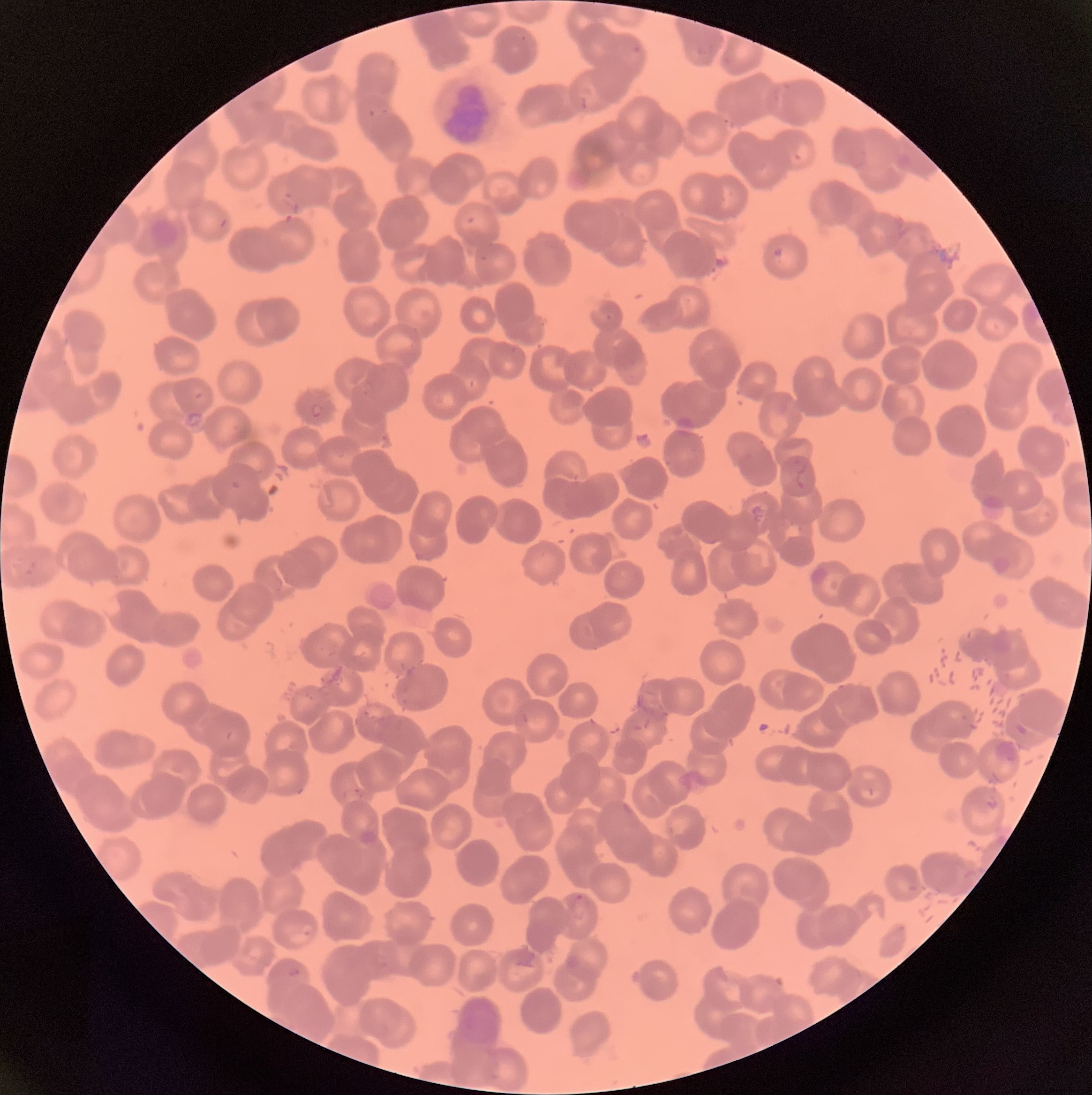

coordinate format = approximate bounding boxes as (x1,y1)-(x2,y2) corner pairs in pixels
Plasmodium parasite locations = (631,44)-(644,57), (368,109)-(376,118), (310,402)-(324,418), (569,893)-(591,920), (288,968)-(300,978)
red blood cell morphology = rouleaux formation
image size = 1092×1095 pixels
preparation = thin blood film
modality = light microscopy